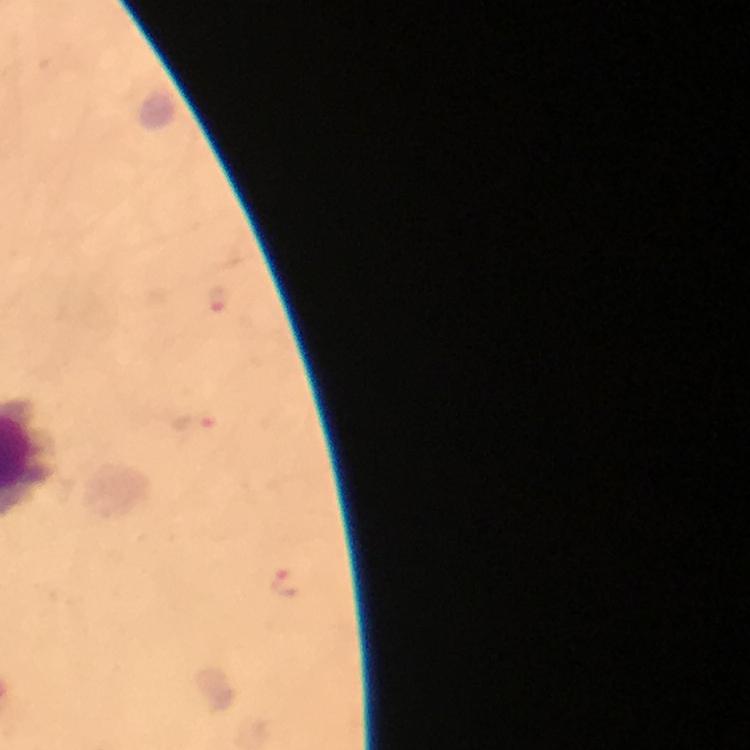
Approximate centers as {x, y} in pixels. Plasmodium parasite locations: {218, 304}, {194, 422}, {285, 585}. At 100x magnification. Immersion oil applied. Cropped region of a single field of view. From a diagnostic examination for malaria. Image is 750×750 pixels. Thick blood film. Photographed through the microscope with a smartphone camera. Giemsa-stained preparation.